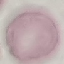 Malaria status: uninfected. Acquired by smartphone through the microscope eyepiece. Thin smear of blood. Automatically extracted cell patch, resized to 64 × 64 pixels. Giemsa-stained preparation.